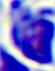

modality = photomicrograph
identification = white blood cell
magnification = 400x